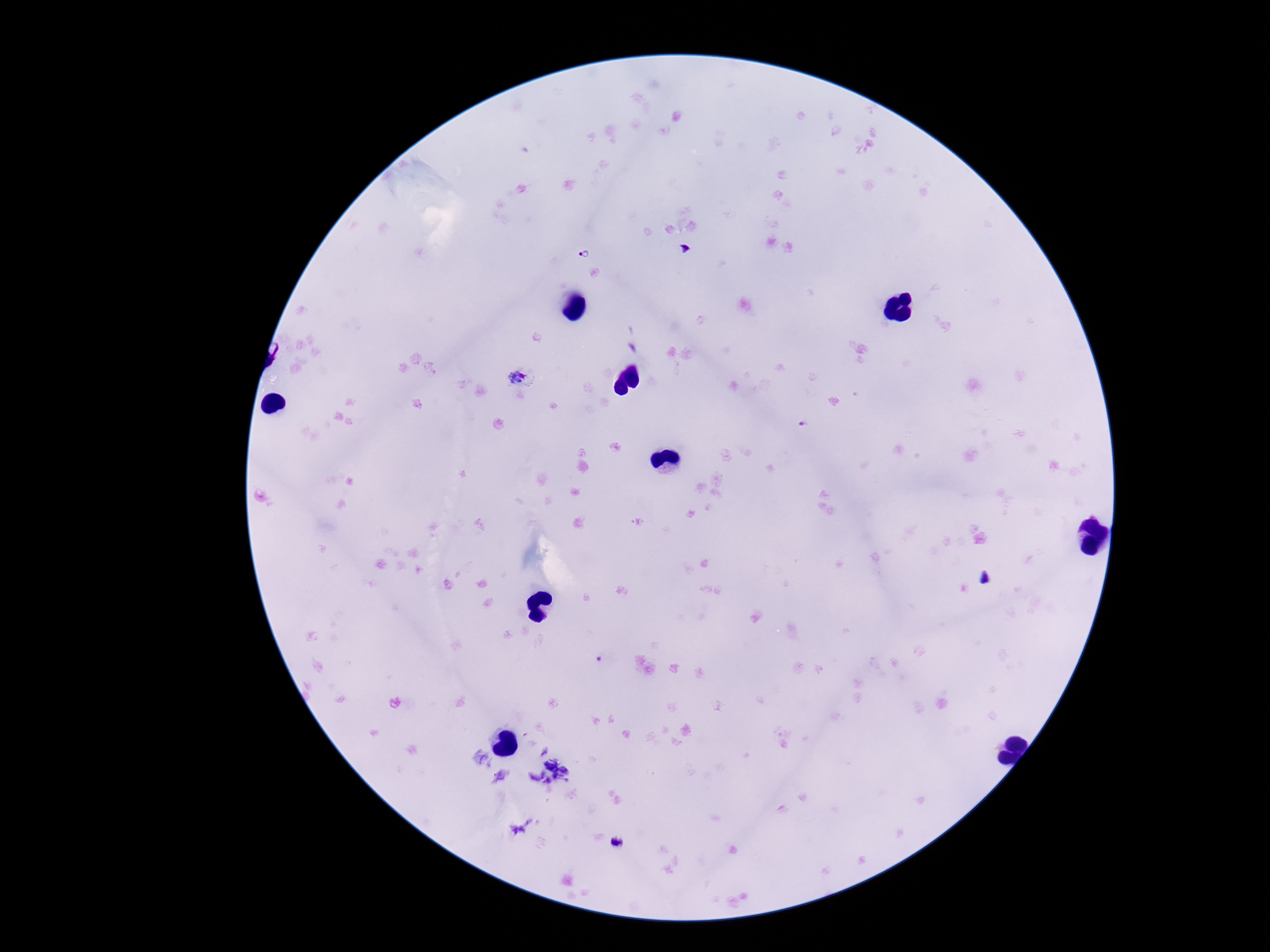
{
  "capture": "smartphone camera through the microscope eyepiece",
  "plasmodium_parasite_locations": "approximate centers as {x, y} in pixels: {585, 252}, {522, 377}, {804, 424}",
  "preparation": "thick peripheral-blood smear",
  "stain": "Giemsa",
  "field_of_view": "single",
  "magnification": "100x",
  "patient_malaria_status": "positive",
  "image_size": "1270×952 pixels"
}